Comment on the morphology of the red blood cells.
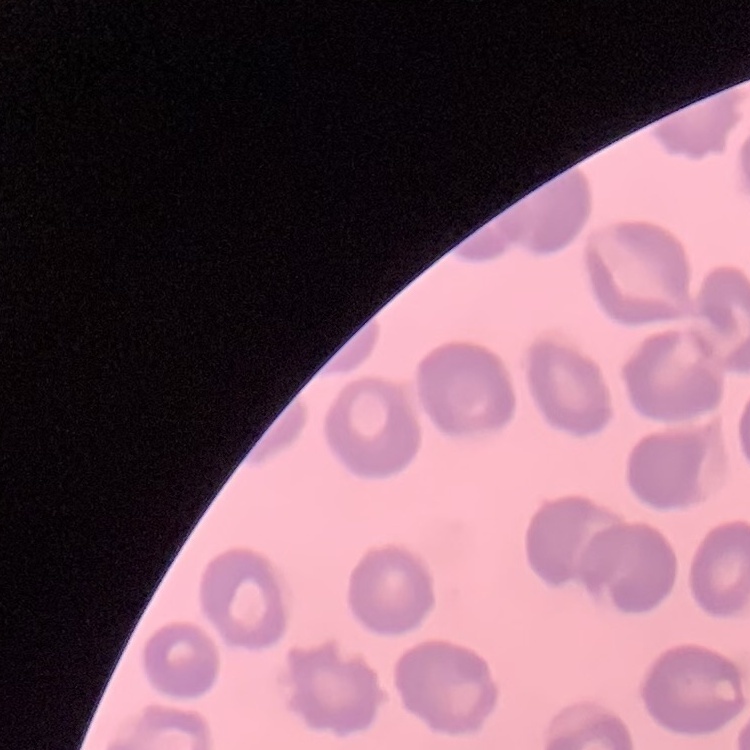

No rouleaux formation.

Summary:
  - Preparation: thin blood film
  - Image type: one tile cut from a larger photomicrograph
  - Stain: Field's or Giemsa